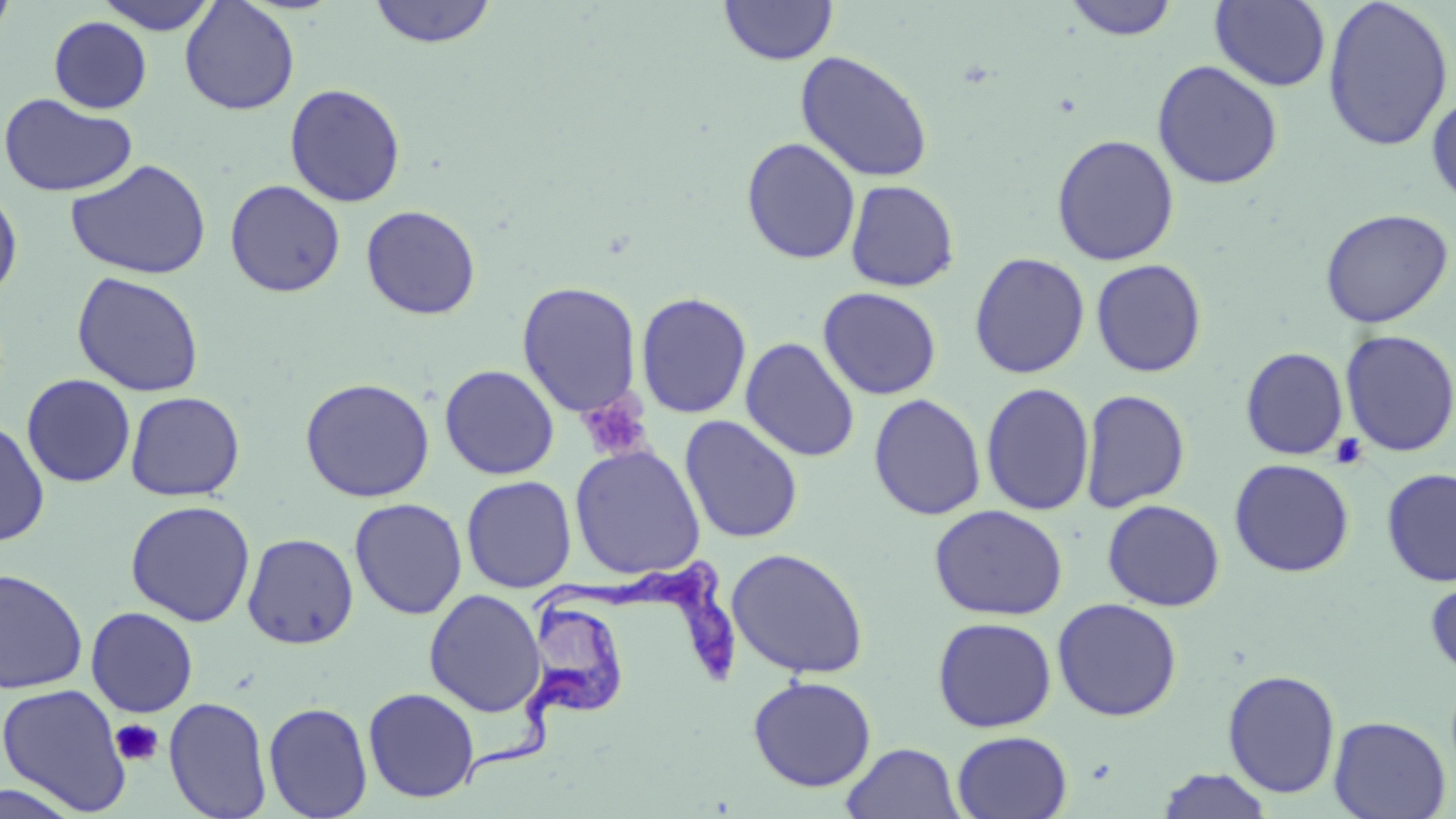
Summary:
  - Coordinate format: approximate bounding boxes as [x1, y1, x2, y2] in pixels
  - Uninfected red blood cell locations: [95, 0, 221, 35], [367, 0, 498, 49], [1063, 0, 1180, 41], [1322, 0, 1454, 152], [0, 1, 18, 46], [179, 1, 300, 115], [719, 1, 838, 66], [1210, 1, 1331, 92], [48, 16, 152, 114], [795, 50, 934, 183], [1151, 60, 1284, 190], [284, 83, 406, 208], [1427, 90, 1456, 207], [0, 92, 138, 198], [1051, 133, 1180, 266], [740, 137, 861, 265], [66, 159, 211, 281], [225, 179, 345, 297], [845, 179, 960, 292], [0, 183, 23, 304], [361, 204, 481, 320], [1319, 208, 1454, 328], [969, 251, 1090, 379], [1090, 258, 1207, 377], [71, 271, 205, 398], [516, 281, 642, 418], [818, 287, 942, 400], [636, 291, 752, 419], [1339, 329, 1456, 458], [740, 337, 860, 462], [1240, 346, 1349, 460], [439, 364, 560, 480], [21, 374, 136, 488], [300, 377, 436, 502], [980, 382, 1095, 517], [1079, 388, 1191, 513], [125, 391, 245, 501], [868, 393, 986, 521], [679, 415, 803, 544], [0, 417, 50, 546], [569, 444, 706, 580], [1228, 458, 1355, 577], [1380, 468, 1456, 587], [461, 475, 577, 593], [349, 498, 467, 620], [1102, 499, 1225, 611], [125, 500, 256, 627], [929, 504, 1068, 620], [242, 532, 359, 650], [726, 547, 869, 680], [0, 567, 89, 695], [1425, 571, 1456, 679], [423, 589, 546, 718], [1052, 597, 1182, 722], [85, 606, 199, 718], [932, 617, 1057, 733], [1222, 668, 1341, 799], [748, 675, 877, 792], [0, 683, 132, 815], [363, 687, 480, 803], [163, 696, 272, 819], [263, 701, 373, 819], [1329, 715, 1451, 818], [951, 730, 1073, 819], [841, 742, 964, 819], [1155, 767, 1274, 818], [0, 778, 86, 818]
  - Platelet locations: [576, 393, 652, 461], [1329, 433, 1368, 470], [110, 718, 163, 766]
  - Trypanosoma brucei locations: [530, 559, 738, 686], [461, 597, 625, 786]
  - Slide-level diagnosis: Trypanosoma brucei
  - Preparation: thin blood smear
  - Image size: 1456×819 pixels
  - Modality: optical microscopy
  - Field of view: single
  - Stain: May-Grünwald-Giemsa
  - Magnification: 1000x